State which parasite is depicted.
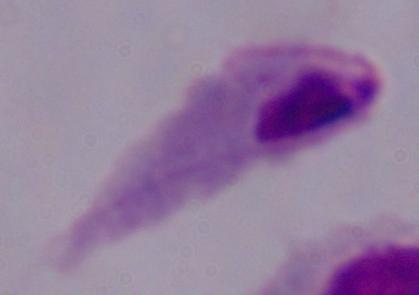
This is a trichomonad.

Summary:
  - Modality: photomicrograph
  - Magnification: 1000x